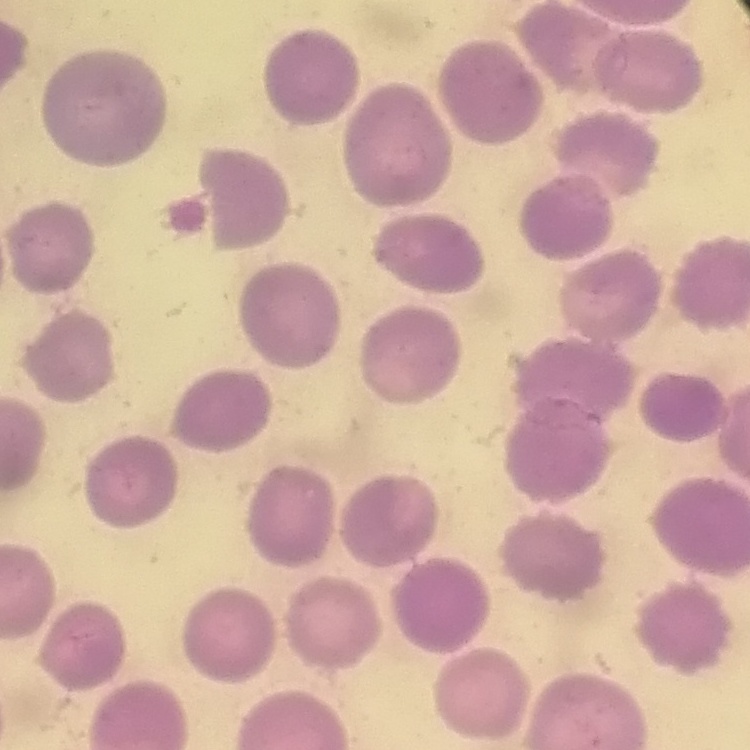

erythrocyte morphology = no rouleaux formation
preparation = thin blood film
image type = one tile cut from a larger photomicrograph
stain = Field's or Giemsa